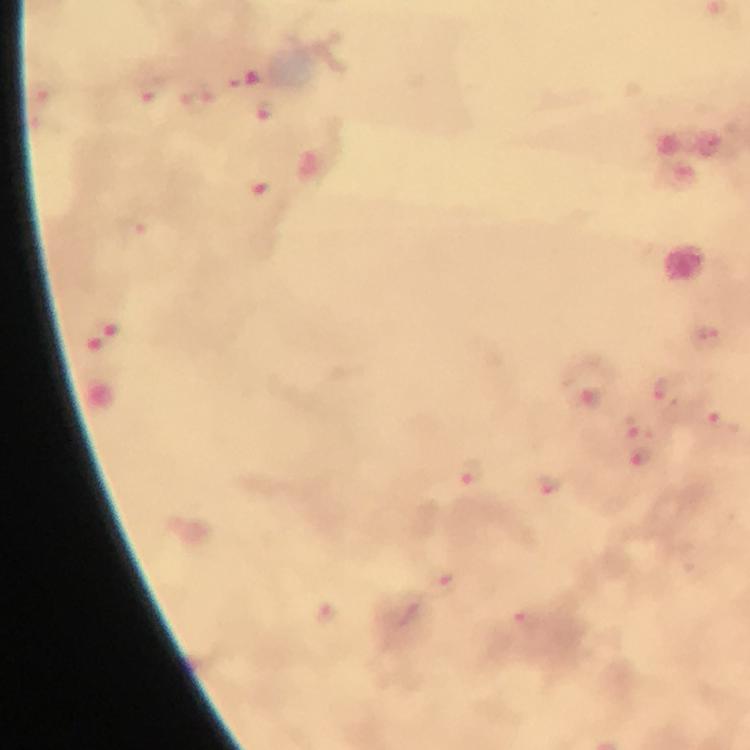
Plasmodium parasite locations = approximate centers as [x, y] in pixels: [151, 91], [265, 110], [660, 389], [586, 398], [634, 425], [722, 426], [642, 455], [470, 474], [553, 484], [443, 582]
preparation = thick blood smear
image size = 750×750 pixels
immersion oil = applied
context = from a malaria diagnostic workup
magnification = 100x
capture = smartphone photograph through a microscope
cropped from = one field of view
stain = Giemsa